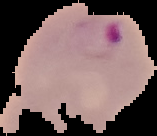

image type = segmented cell region on a black background
image size = 157×136 pixels
result = malaria parasites identified
preparation = thin blood film